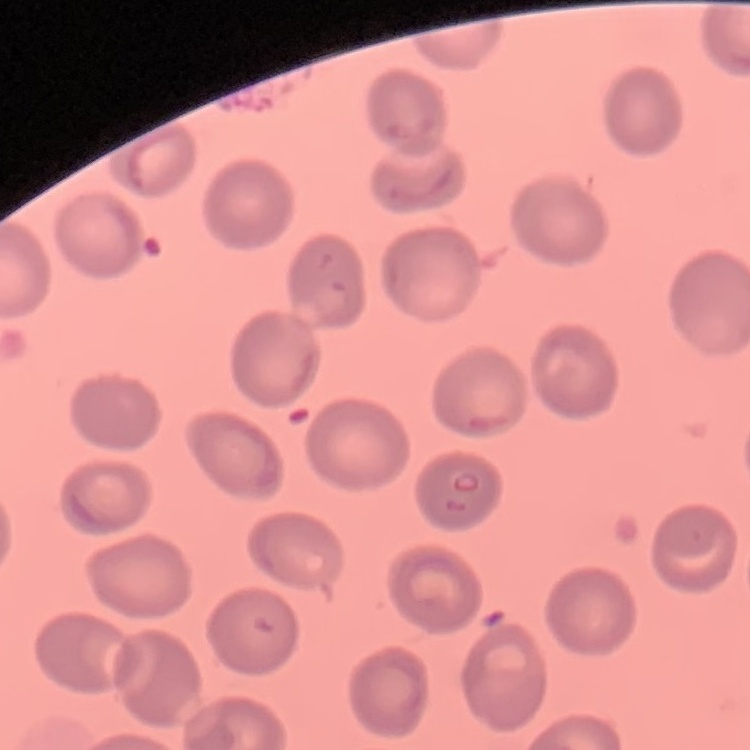

red_blood_cell_morphology: no rouleaux formation
stain: Field's or Giemsa
preparation: thin blood film
image_type: one tile cut from a larger photomicrograph